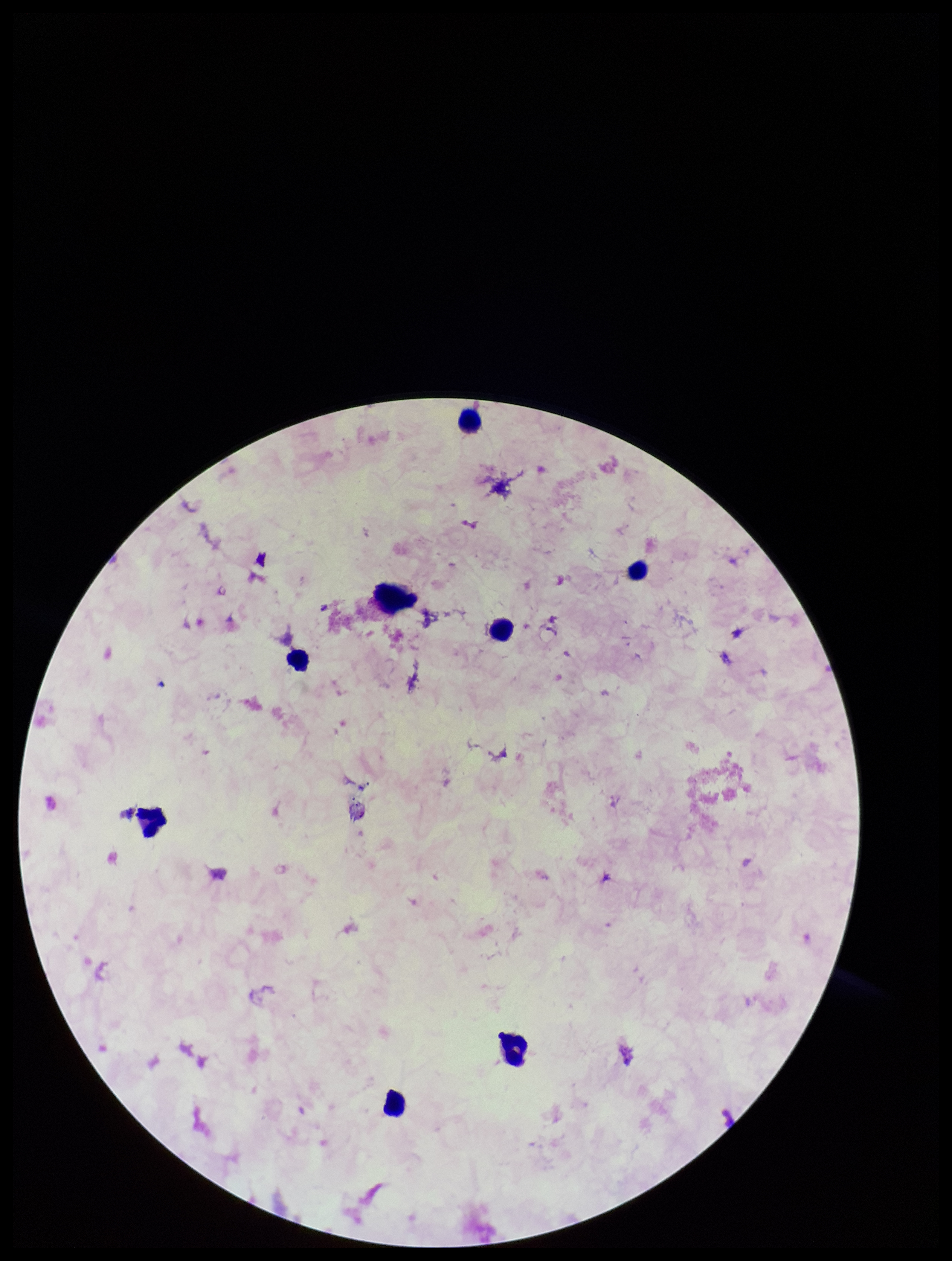

{
  "parasite_count": 0,
  "leukocyte_count": 7,
  "plasmodium_parasites": "none detected",
  "preparation": "thick",
  "capture": "smartphone photograph through the microscope eyepiece",
  "image_size": "952×1261 pixels",
  "patient_malaria_status": "negative",
  "field_of_view": "one from this slide",
  "stain": "Giemsa"
}